Classify this cell by malaria status.
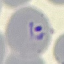
It is parasitized.

Summary:
  - Stain: Giemsa
  - Image type: automatically extracted cell patch, resized to 64 × 64 pixels
  - Preparation: thin blood smear
  - Capture: smartphone camera at the microscope eyepiece